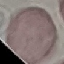

result = negative for malaria parasites
stain = Giemsa
image type = cell patch, automatically extracted from a larger field of view and resized to 64 × 64 pixels
preparation = thin smear
capture = smartphone camera at the microscope eyepiece